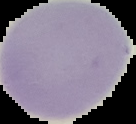

Summary:
  - Result: no Plasmodium parasites seen
  - Image size: 136×124 pixels
  - Image type: segmented cell region on a black background
  - Preparation: thin blood film